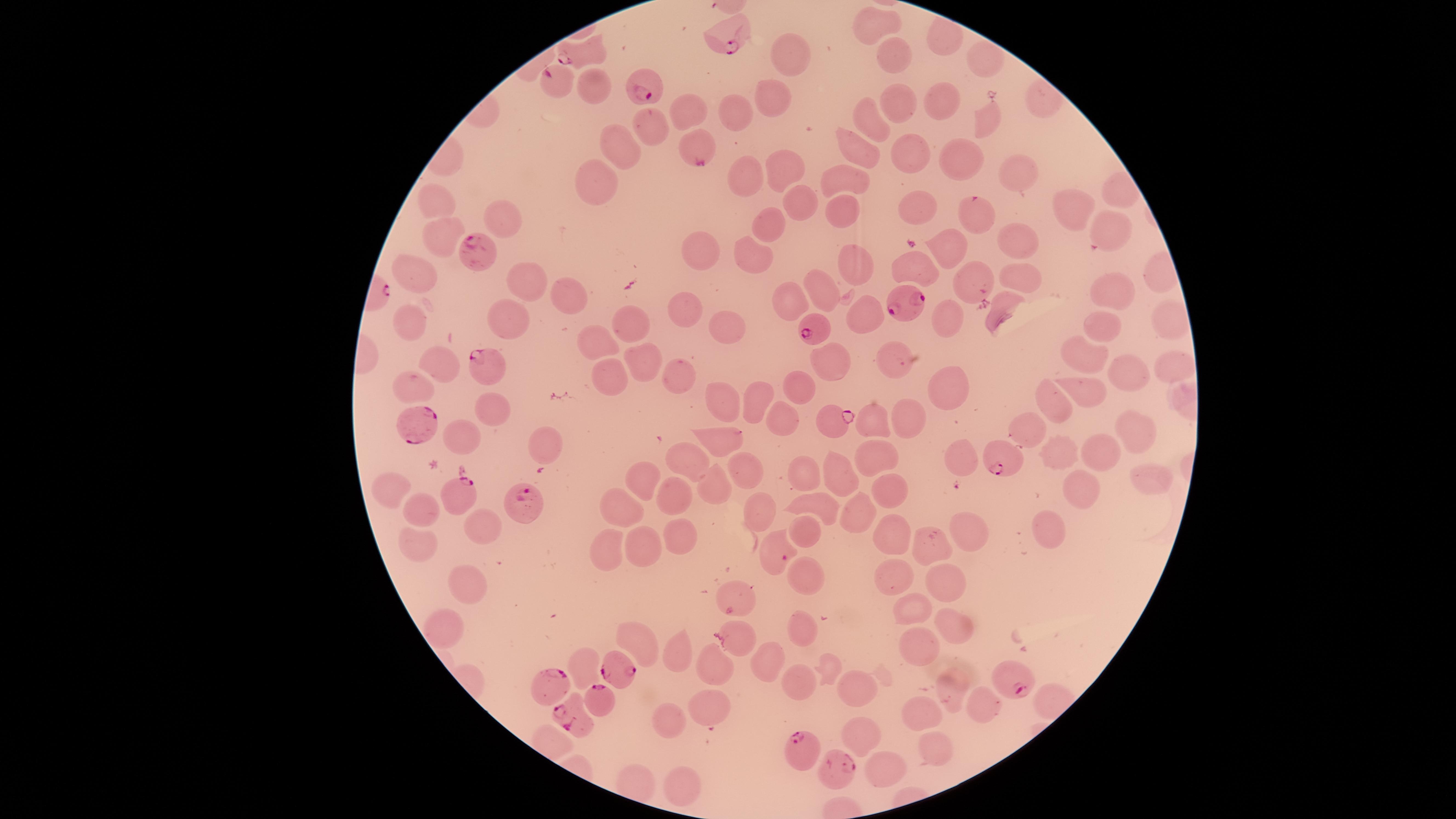

Approximate marker points, in pixels from the top-left corner.
Summary:
  - Uninfected RBCs: (x=875, y=19), (x=782, y=48), (x=897, y=54), (x=982, y=58), (x=596, y=86), (x=765, y=96), (x=943, y=97), (x=899, y=98), (x=734, y=109), (x=691, y=110), (x=875, y=115), (x=652, y=127), (x=618, y=141), (x=860, y=144), (x=899, y=144), (x=955, y=158), (x=781, y=168), (x=1019, y=171), (x=744, y=177), (x=849, y=177), (x=598, y=186), (x=435, y=200), (x=799, y=200), (x=919, y=203), (x=1070, y=205), (x=849, y=208), (x=973, y=212), (x=502, y=216), (x=771, y=227), (x=1107, y=228), (x=439, y=237), (x=1020, y=241), (x=952, y=243), (x=693, y=247), (x=752, y=255), (x=860, y=262), (x=918, y=263), (x=1015, y=274), (x=972, y=280), (x=416, y=282), (x=523, y=283), (x=825, y=283), (x=566, y=294), (x=1115, y=294), (x=792, y=300), (x=685, y=306), (x=997, y=311), (x=1164, y=314), (x=865, y=317), (x=950, y=318), (x=503, y=319), (x=1105, y=322), (x=630, y=323), (x=407, y=327), (x=728, y=328), (x=603, y=339), (x=1087, y=355), (x=827, y=358), (x=443, y=360), (x=644, y=360), (x=887, y=361), (x=1171, y=362), (x=1120, y=373), (x=613, y=378), (x=678, y=378), (x=802, y=379), (x=958, y=380), (x=414, y=384), (x=1091, y=387), (x=750, y=393), (x=718, y=397), (x=1054, y=400), (x=490, y=410), (x=782, y=410), (x=909, y=418), (x=870, y=422), (x=1030, y=426), (x=461, y=432), (x=1132, y=432), (x=726, y=438), (x=543, y=442), (x=1061, y=452), (x=1102, y=453), (x=870, y=455), (x=964, y=457), (x=696, y=465), (x=801, y=469), (x=838, y=475), (x=749, y=476), (x=1141, y=478), (x=649, y=483), (x=885, y=483), (x=713, y=485), (x=388, y=486), (x=1080, y=488), (x=670, y=493), (x=424, y=504), (x=819, y=506), (x=625, y=507), (x=855, y=515), (x=757, y=516), (x=1045, y=523), (x=487, y=524), (x=805, y=532), (x=970, y=533), (x=891, y=534), (x=679, y=537), (x=418, y=542), (x=646, y=543), (x=930, y=546), (x=610, y=547), (x=890, y=566), (x=806, y=578), (x=947, y=581), (x=474, y=586), (x=736, y=592), (x=918, y=607), (x=952, y=620), (x=735, y=625), (x=444, y=627), (x=801, y=628), (x=635, y=636), (x=918, y=645), (x=674, y=650), (x=768, y=659), (x=718, y=664), (x=588, y=666), (x=831, y=667), (x=800, y=681), (x=852, y=689), (x=952, y=689), (x=711, y=701), (x=986, y=702), (x=925, y=712), (x=666, y=723), (x=856, y=729), (x=937, y=748), (x=876, y=764), (x=681, y=784)
  - Parasitized RBCs: (x=736, y=39), (x=578, y=52), (x=558, y=83), (x=655, y=89), (x=700, y=162), (x=472, y=255), (x=908, y=300), (x=817, y=331), (x=480, y=362), (x=832, y=418), (x=419, y=423), (x=1010, y=460), (x=462, y=495), (x=532, y=503), (x=780, y=553), (x=617, y=668), (x=1017, y=680), (x=551, y=687), (x=598, y=701), (x=578, y=718), (x=802, y=746), (x=839, y=764)
  - Image size: 1456×819 pixels
  - Field of view: single
  - Species: Plasmodium falciparum
  - Preparation: thin smear of blood
  - Capture: smartphone photograph through the microscope eyepiece
  - Visible region: circular
  - Stain: Giemsa
  - Presence: malaria parasites seen